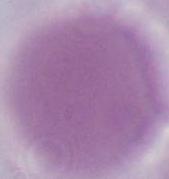

An erythrocyte is seen. Captured at 1000x magnification. Photomicrograph.